Identify the parasite.
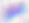
This is Toxoplasma gondii.

magnification: 400x
modality: photomicrograph